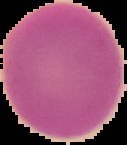

malaria status = uninfected
image type = segmented cell region with the area outside set to black
preparation = thin blood film
image size = 127×145 pixels